Locate every malaria parasite.
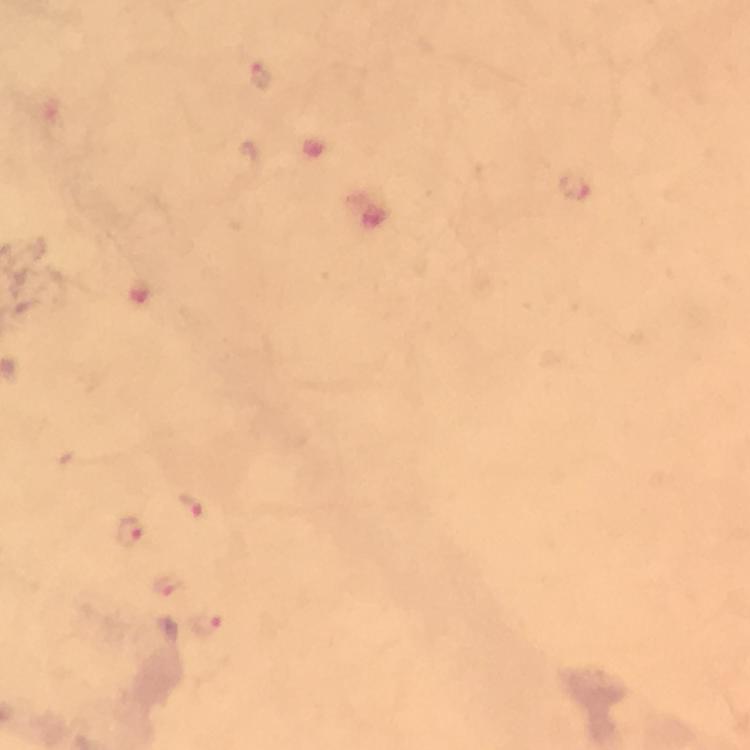

Approximate centers as [x, y] in pixels.
Malaria parasites: [260, 78], [576, 187], [193, 504], [131, 533].

Summary:
  - Cropped from: one field of view
  - Image size: 750×750 pixels
  - Stain: Giemsa
  - Context: from a diagnostic examination for malaria
  - Preparation: thick blood smear
  - Immersion oil: applied
  - Magnification: 100x
  - Capture: smartphone photograph through a microscope